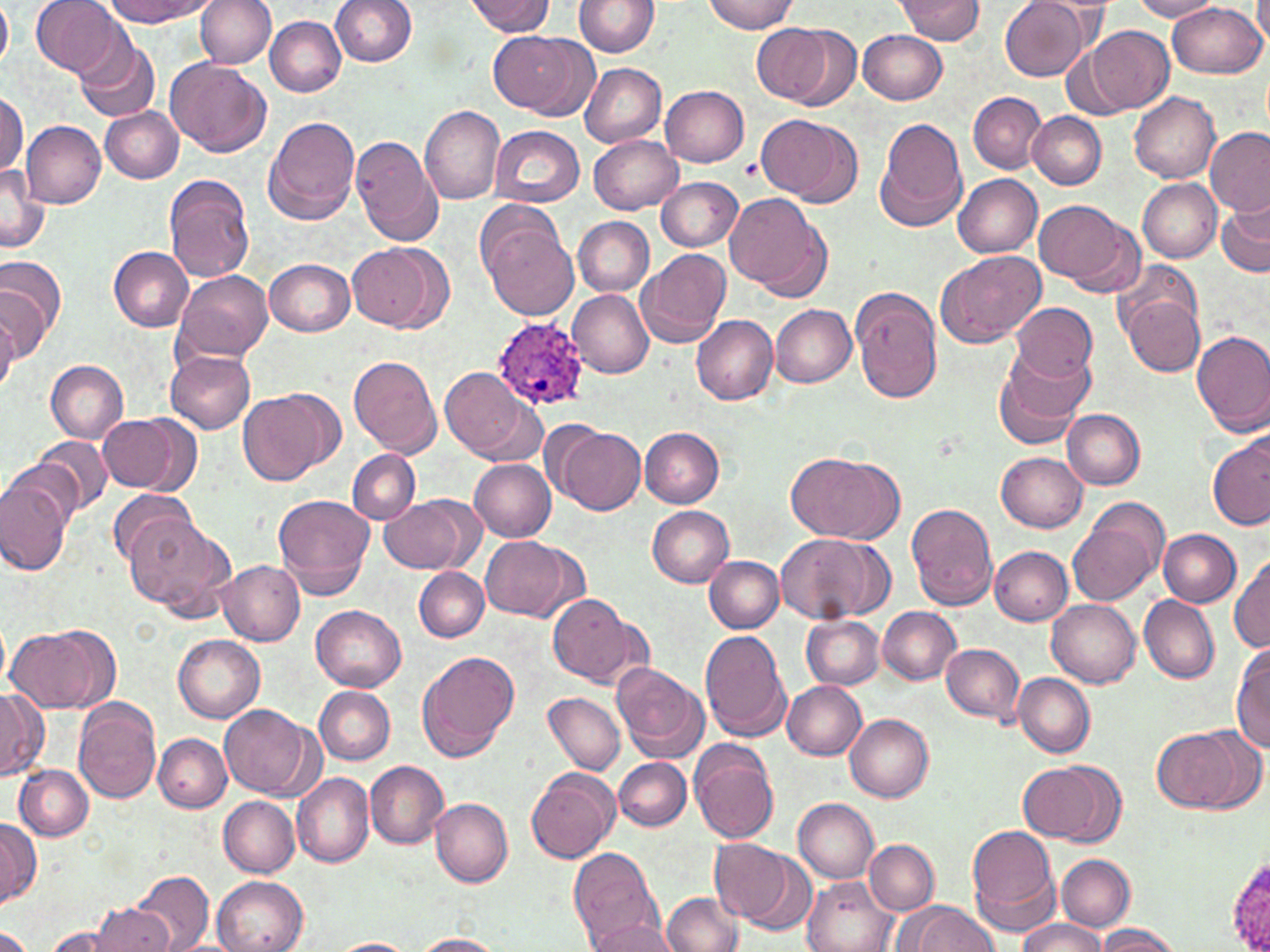

{
  "slide_level_diagnosis": "Plasmodium ovale",
  "field_of_view": "one of a larger specimen",
  "image_size": "1270×952 pixels",
  "preparation": "thin blood smear",
  "plasmodium_ovale_infected_red_blood_cell_locations": "approximate bounding boxes as [x1, y1, x2, y2] in pixels: [492, 315, 589, 410]",
  "magnification": "1000x",
  "modality": "light microscopy",
  "stain": "May-Grünwald-Giemsa",
  "uninfected_red_blood_cell_locations": "approximate bounding boxes as [x1, y1, x2, y2] in pixels: [0, 0, 12, 73], [103, 0, 214, 26], [195, 0, 275, 68], [331, 0, 417, 67], [574, 0, 659, 56], [702, 0, 799, 34], [894, 0, 987, 43], [1000, 0, 1093, 82], [1132, 0, 1222, 21], [1254, 0, 1270, 50], [31, 1, 125, 77], [464, 1, 555, 36], [1168, 3, 1265, 79], [266, 16, 345, 96], [751, 22, 846, 108], [1087, 25, 1174, 113], [858, 30, 947, 104], [492, 31, 593, 118], [74, 35, 159, 122], [167, 57, 271, 157], [580, 63, 666, 147], [660, 85, 749, 166], [967, 91, 1046, 174], [1128, 91, 1221, 183], [0, 92, 26, 177], [420, 105, 505, 204], [101, 107, 183, 183], [1028, 111, 1106, 190], [757, 113, 861, 207], [262, 114, 360, 226], [876, 114, 970, 233], [21, 119, 106, 208], [488, 125, 584, 209], [1204, 125, 1270, 215], [589, 134, 683, 214], [351, 136, 443, 247], [0, 165, 49, 255], [952, 173, 1042, 257], [164, 175, 254, 282], [657, 177, 744, 251], [1138, 178, 1222, 262], [725, 193, 829, 298], [1217, 197, 1269, 278], [1033, 199, 1140, 295], [480, 214, 579, 321], [573, 216, 653, 297], [348, 242, 448, 334], [109, 247, 194, 332], [934, 248, 1047, 347], [636, 249, 730, 348], [0, 254, 66, 348], [264, 258, 355, 336], [173, 271, 273, 363], [1, 282, 49, 366], [1119, 282, 1206, 379], [850, 285, 944, 403], [567, 289, 654, 378], [1008, 301, 1096, 385], [770, 305, 857, 388], [0, 307, 18, 396], [692, 314, 778, 405], [1192, 328, 1270, 437], [993, 346, 1094, 449], [166, 350, 256, 434], [347, 355, 442, 458], [45, 360, 129, 443], [441, 367, 540, 465], [240, 389, 338, 486], [1063, 409, 1146, 489], [99, 414, 192, 494], [554, 426, 645, 513], [639, 427, 725, 507], [1207, 434, 1270, 531], [33, 437, 113, 515], [5, 449, 94, 533], [786, 449, 903, 543], [347, 450, 421, 524], [997, 452, 1088, 532], [470, 459, 556, 542], [1, 476, 75, 575], [108, 487, 197, 571], [381, 493, 481, 574], [273, 494, 377, 600], [1067, 498, 1168, 608], [906, 502, 1001, 611], [647, 505, 735, 588], [123, 513, 236, 612], [1158, 529, 1241, 606], [774, 533, 892, 626], [479, 536, 581, 620], [989, 547, 1072, 625], [704, 555, 783, 631], [1230, 555, 1270, 654], [217, 559, 305, 645], [415, 569, 489, 642], [548, 593, 643, 687], [1140, 596, 1220, 684], [1046, 598, 1141, 688], [311, 603, 406, 691], [877, 606, 961, 684], [802, 615, 884, 690], [7, 628, 107, 714], [699, 630, 790, 742], [172, 634, 265, 724], [1231, 641, 1270, 755], [942, 642, 1025, 725], [417, 651, 520, 762], [612, 662, 709, 764], [1014, 673, 1095, 757], [781, 680, 867, 759], [315, 686, 395, 765], [0, 688, 48, 780], [544, 692, 625, 776], [72, 698, 162, 803], [221, 705, 317, 800], [843, 714, 935, 802], [1151, 725, 1255, 813], [154, 734, 232, 813], [689, 739, 781, 844], [614, 758, 690, 830], [1018, 760, 1119, 844], [365, 761, 448, 847], [15, 763, 95, 842], [526, 767, 621, 864], [292, 772, 372, 868], [219, 796, 299, 877], [430, 797, 513, 887], [793, 797, 879, 882], [0, 818, 40, 907], [967, 823, 1061, 932], [711, 839, 796, 924], [865, 840, 939, 915], [567, 846, 661, 948], [1227, 850, 1270, 952], [1057, 854, 1134, 931], [130, 871, 213, 952], [212, 875, 308, 952], [802, 877, 896, 952], [660, 890, 744, 951], [897, 901, 1001, 952], [91, 903, 172, 952], [585, 914, 680, 952], [1016, 918, 1107, 952], [44, 923, 128, 952], [1093, 924, 1184, 952], [0, 927, 35, 952], [412, 934, 504, 952], [329, 938, 419, 952]"
}